Give the position of every leukocyte visible.
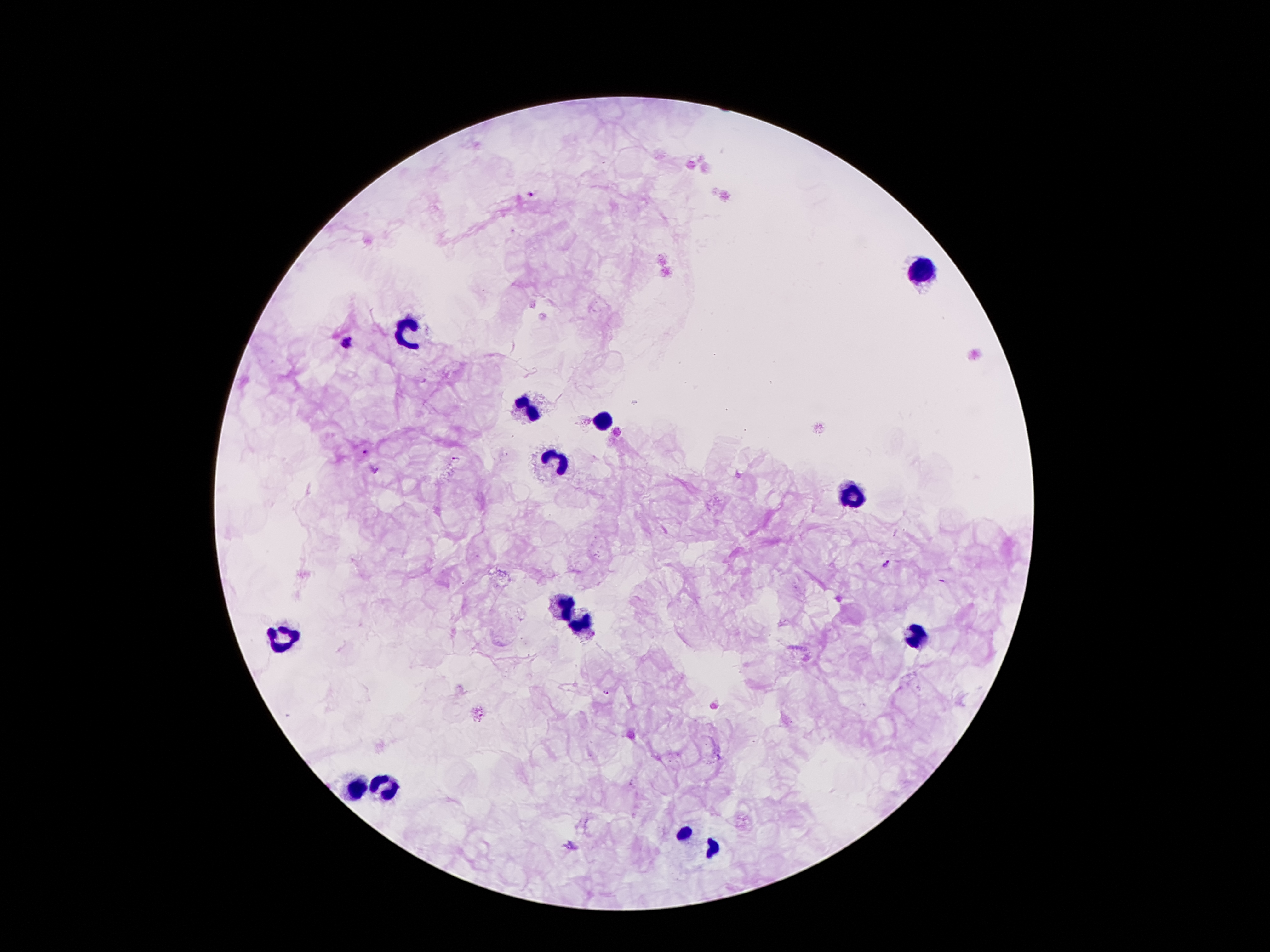
Approximate centers as [x, y] in pixels.
Leukocytes: [923, 268], [407, 329], [531, 409], [604, 419], [558, 463], [852, 490], [566, 608], [583, 623], [919, 635], [281, 637], [358, 790], [386, 790], [687, 832], [714, 847].

Plasmodium parasite locations: [532, 195], [346, 340], [364, 451], [456, 459], [887, 565], [606, 692]. Image is 1270×952 pixels. Single field of view. Thick peripheral-blood smear. Giemsa stain. Patient malaria status: infected with Plasmodium falciparum. 100x magnification. Smartphone photograph taken through the microscope eyepiece.